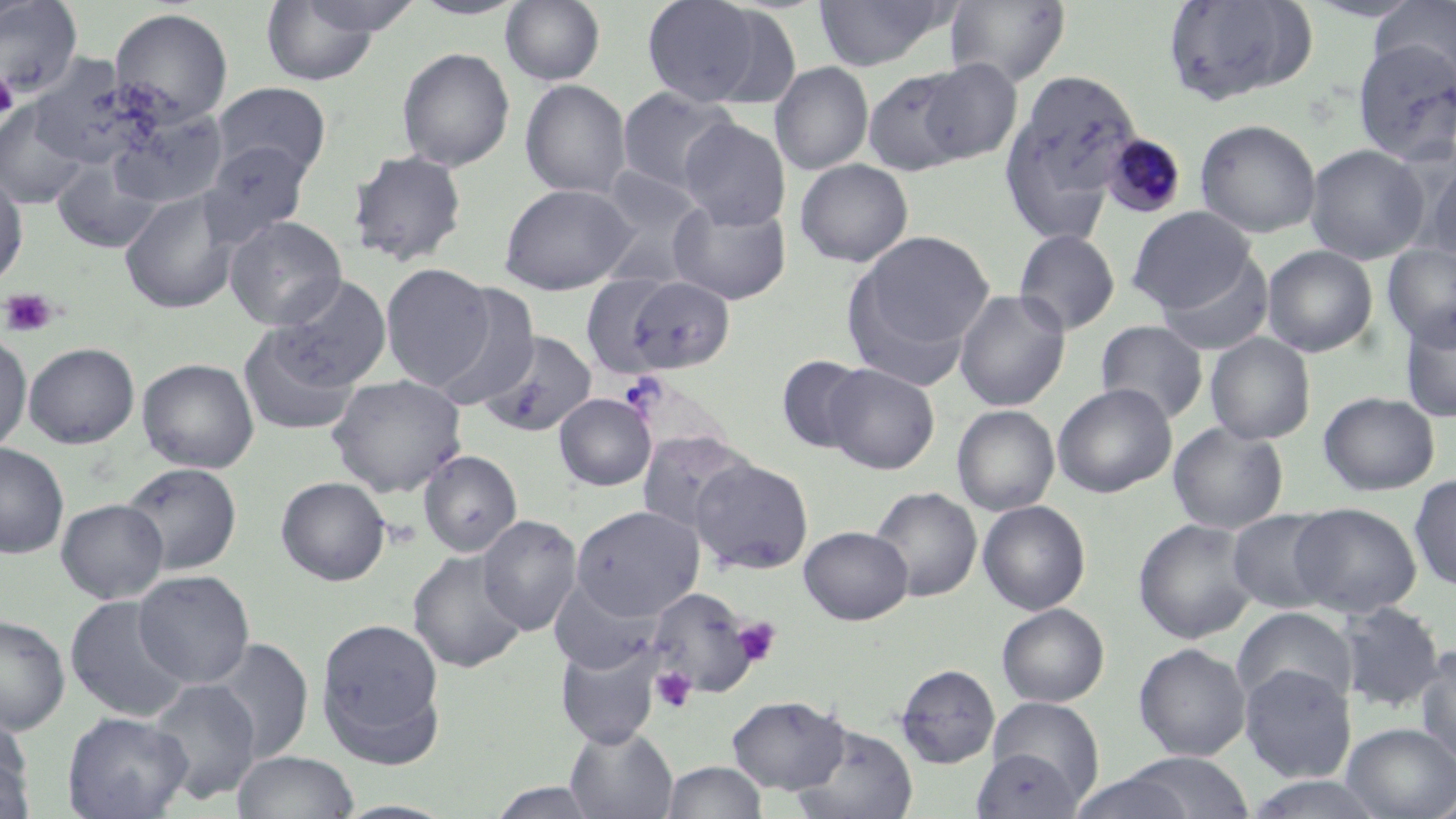

slide-level diagnosis = Plasmodium malariae
stain = May-Grünwald-Giemsa
modality = light microscopy
preparation = thin blood film
uninfected red blood cell locations = approximate bounding boxes as (x1,y1)-(x2,y2) corner pairs in pixels: (297,0)-(423,37), (410,0)-(529,20), (500,0)-(606,86), (641,0)-(769,105), (813,0)-(954,71), (1162,0)-(1318,106), (0,1)-(84,98), (261,1)-(383,86), (945,1)-(1071,88), (1371,1)-(1456,88), (704,5)-(806,111), (109,8)-(234,127), (1352,40)-(1456,167), (397,47)-(514,171), (35,51)-(147,164), (914,58)-(1022,164), (770,62)-(874,176), (862,67)-(979,176), (999,68)-(1142,238), (520,79)-(632,200), (213,82)-(332,182), (616,86)-(740,196), (1,100)-(93,209), (109,111)-(228,209), (678,118)-(790,230), (1195,118)-(1321,238), (200,142)-(311,246), (1305,144)-(1430,264), (347,150)-(468,267), (52,158)-(164,255), (794,158)-(913,268), (1422,158)-(1456,270), (591,167)-(710,288), (0,170)-(29,288), (499,183)-(636,295), (119,189)-(241,314), (668,196)-(792,305), (1127,206)-(1255,314), (225,216)-(346,330), (1013,229)-(1120,336), (846,230)-(993,373), (1383,243)-(1456,349), (1262,245)-(1378,357), (1157,254)-(1274,357), (380,263)-(496,391), (269,275)-(391,390), (607,275)-(738,376), (430,286)-(540,411), (954,288)-(1071,411), (1399,308)-(1456,423), (1096,320)-(1208,425), (239,325)-(361,436), (0,330)-(32,454), (479,330)-(597,438), (1205,333)-(1316,446), (24,342)-(140,449), (775,355)-(871,455), (137,358)-(259,473), (823,363)-(939,474), (327,374)-(467,497), (1052,383)-(1177,498), (1318,391)-(1440,496), (554,393)-(656,491), (952,405)-(1060,516), (1168,421)-(1288,534), (636,430)-(757,539), (0,442)-(69,558), (419,450)-(522,556), (689,458)-(814,576), (119,461)-(243,576), (1409,474)-(1456,591), (275,476)-(392,586), (869,486)-(982,602), (56,498)-(169,603), (977,500)-(1091,616), (1289,502)-(1422,617), (571,505)-(704,620), (1227,509)-(1341,613), (477,515)-(583,636), (1133,517)-(1260,644), (799,525)-(913,625), (407,550)-(528,673), (133,570)-(255,689), (550,577)-(663,674), (647,587)-(758,698), (65,596)-(192,723), (1338,601)-(1446,713), (996,603)-(1110,707), (1232,607)-(1357,710), (0,614)-(70,735), (316,617)-(446,764), (209,639)-(313,764), (556,643)-(659,747), (1134,643)-(1252,761), (1414,647)-(1456,770), (896,663)-(1000,767), (1240,664)-(1356,783), (147,679)-(261,804), (726,695)-(851,794), (985,696)-(1104,810), (62,711)-(192,819), (0,722)-(35,819), (791,723)-(918,819), (1341,723)-(1456,818), (566,726)-(678,819), (972,749)-(1086,818), (232,750)-(359,819), (1118,751)-(1256,818), (662,760)-(768,819), (1067,772)-(1197,819), (1242,775)-(1391,818), (486,781)-(604,819), (1426,786)-(1456,819), (332,799)-(459,818)
image size = 1456×819 pixels
Plasmodium malariae-infected red blood cell locations = approximate bounding boxes as (x1,y1)-(x2,y2) corner pairs in pixels: (1102,133)-(1187,219)
magnification = 1000x
field of view = single
platelet locations = approximate bounding boxes as (x1,y1)-(x2,y2) corner pairs in pixels: (0,70)-(18,121), (1,287)-(57,337), (733,617)-(782,666), (650,667)-(697,713)